Assess the morphology of the red blood cells.
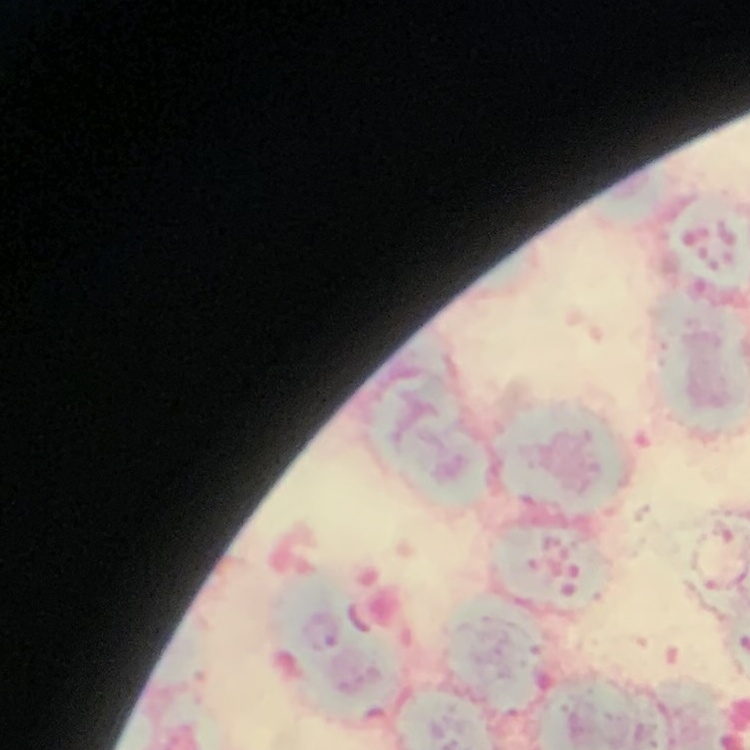
Rouleaux formation.

preparation = thin blood smear
stain = Field's or Giemsa
image type = square crop of a larger photomicrograph